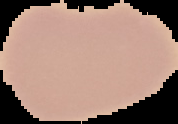
Cell region segmented out of the field of view; the surrounding area is masked to black. From a thin blood smear. Malaria status: uninfected. Image is 178×124 pixels.